Classify this cell by malaria status.
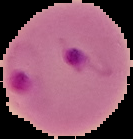
Parasitized.

Summary:
  - Image type: cell region segmented out of the field of view; surrounding area masked to black
  - Image size: 133×139 pixels
  - Preparation: thin blood film